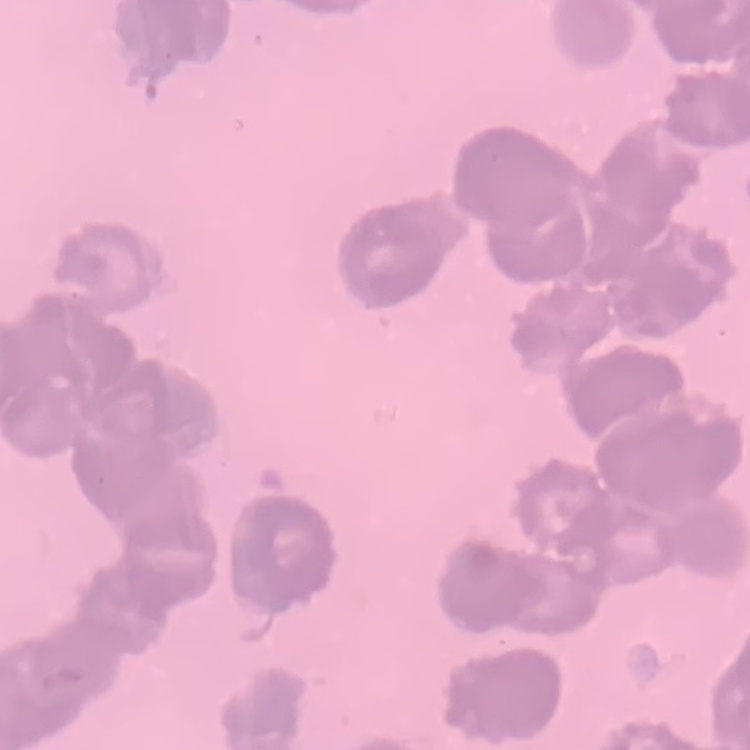
{
  "erythrocyte_morphology": "rouleaux formation",
  "preparation": "thin blood film",
  "image_type": "square crop of a larger photomicrograph",
  "stain": "Field's or Giemsa"
}